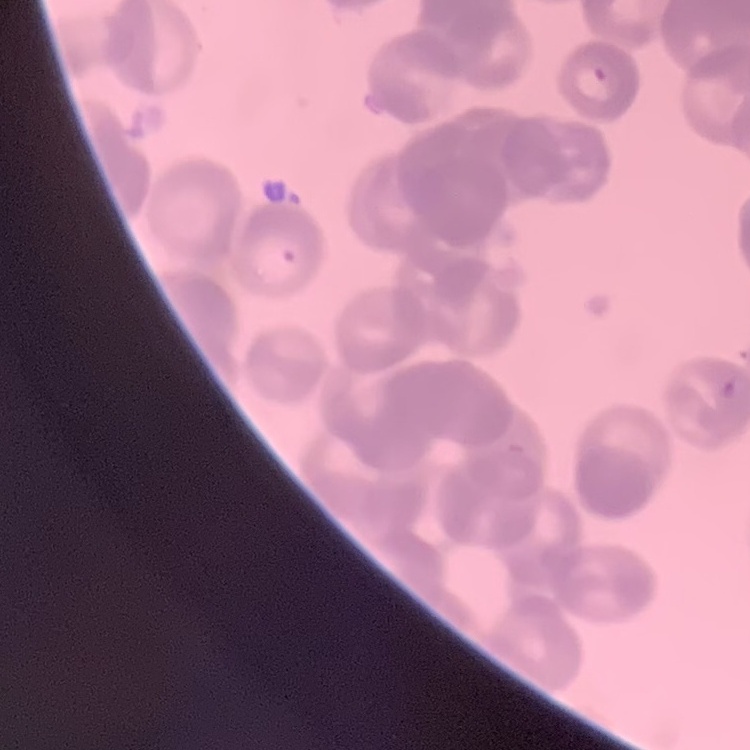
red blood cell morphology = rouleaux formation
stain = Field's or Giemsa
preparation = thin blood smear
image type = one tile cut from a larger photomicrograph